State which parasite is depicted.
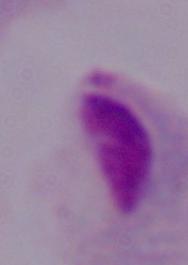
This is a trichomonad.

modality = micrograph
magnification = 1000x